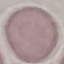
Summary:
  - Malaria status: uninfected
  - Stain: Giemsa
  - Preparation: thin smear
  - Image type: cell patch, automatically extracted from a larger field of view and resized to 64 × 64 pixels
  - Capture: smartphone camera at the microscope eyepiece